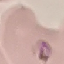
malaria status = parasitized
stain = Giemsa
preparation = thin blood smear
image type = automatically extracted cell patch, resized to 64 × 64 pixels
capture = smartphone through the microscope eyepiece